Report the malaria status of this cell.
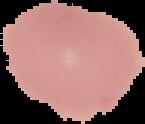

It is uninfected.

From a thin blood film. Cell region segmented out of the field of view; the surrounding area is masked to black. Image is 145×124 pixels.